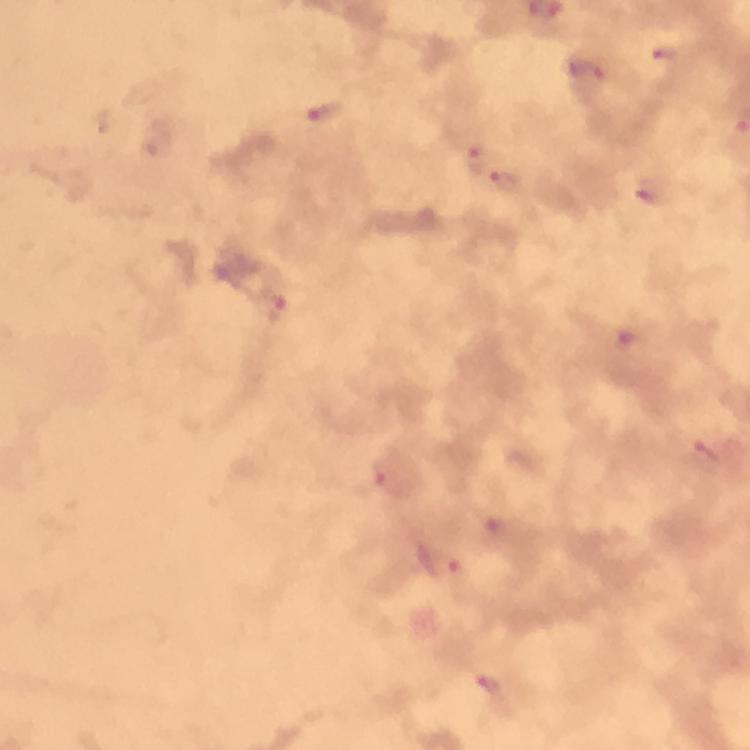
Approximate object centers, in pixels from the top-left corner.
Summary:
  - Malaria parasite locations: (x=663, y=57), (x=590, y=75), (x=324, y=111), (x=475, y=158), (x=506, y=183), (x=649, y=194), (x=275, y=310), (x=630, y=338), (x=702, y=454), (x=390, y=474), (x=494, y=529), (x=442, y=566), (x=490, y=686)
  - Magnification: 100x
  - Cropped from: one field of view
  - Image size: 750×750 pixels
  - Immersion oil: applied
  - Context: from a diagnostic examination for malaria
  - Capture: smartphone camera through the microscope
  - Stain: Giemsa
  - Preparation: thick blood smear